Give the position of every leukocyte visible.
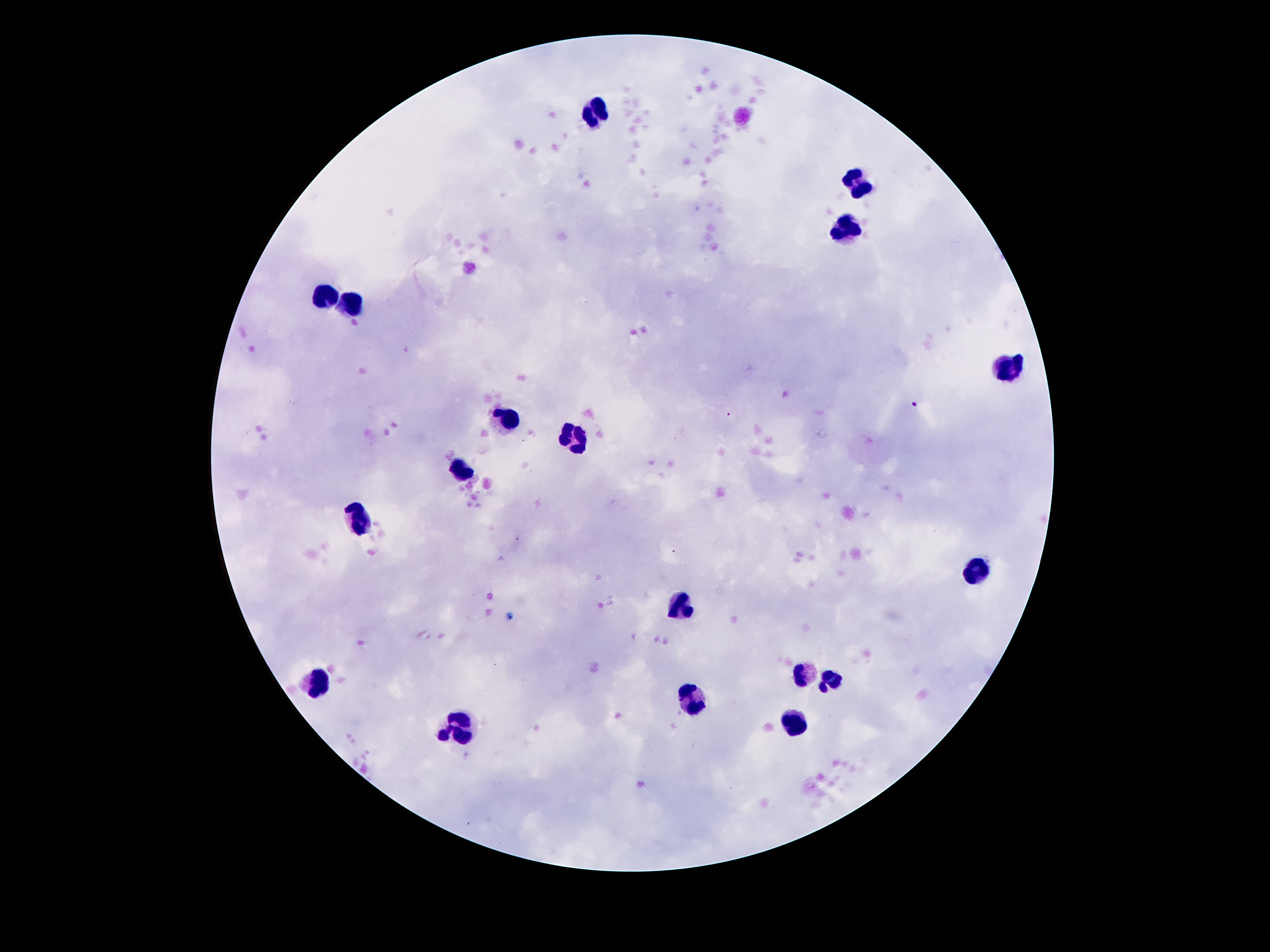

Approximate centers as {x, y} in pixels.
Leukocytes: {596, 110}, {856, 180}, {846, 228}, {324, 294}, {352, 301}, {1013, 366}, {510, 421}, {574, 439}, {462, 472}, {359, 521}, {979, 569}, {680, 606}, {804, 674}, {830, 682}, {314, 684}, {693, 699}, {796, 722}, {458, 727}.

patient malaria status = not infected
preparation = thick peripheral-blood smear
stain = Giemsa
capture = smartphone camera through the microscope eyepiece
image size = 1270×952 pixels
magnification = 100x
field of view = one from this slide